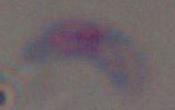 1000x magnification. Toxoplasma gondii is seen. Photomicrograph.